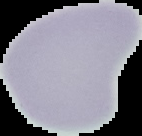
image size = 142×136 pixels
preparation = thin blood smear
image type = cell region segmented out of the field of view; surrounding area masked to black
malaria status = uninfected